Locate and identify every blood parasite.
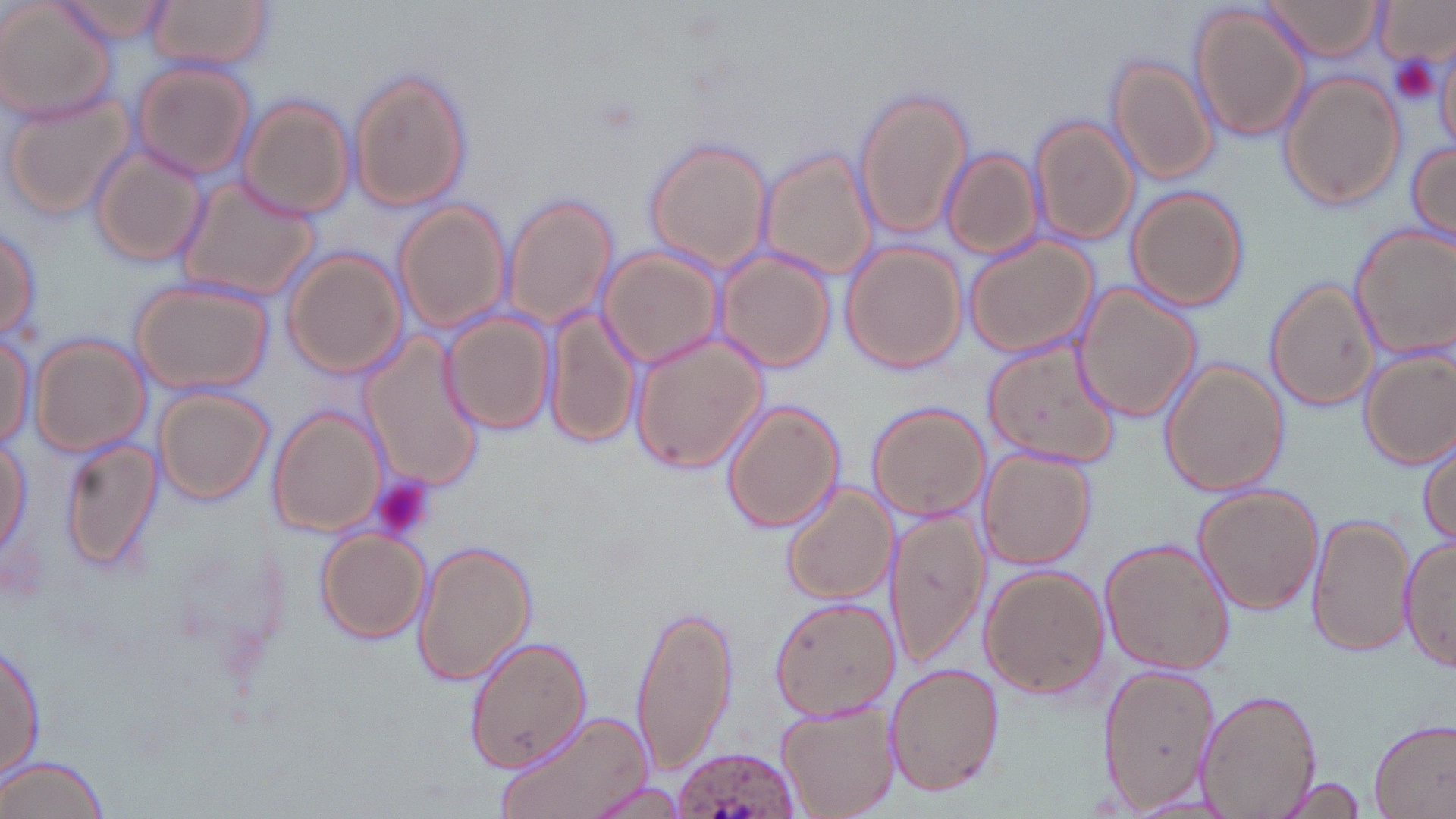
Approximate bounding boxes as (x1, y1, x2, y2) in pixels.
Plasmodium ovale-infected red blood cells: (671, 743, 803, 819).
No Plasmodium falciparum, Plasmodium malariae, Plasmodium vivax, Babesia divergens, or Trypanosoma brucei observed.

Summary:
  - Platelet locations: (1390, 55, 1441, 105), (370, 477, 437, 543)
  - Uninfected red blood cell locations: (149, 0, 271, 71), (1259, 0, 1386, 62), (0, 2, 118, 124), (59, 2, 173, 47), (1374, 2, 1452, 67), (1187, 3, 1312, 143), (1106, 53, 1219, 187), (130, 58, 258, 180), (346, 67, 473, 213), (1278, 71, 1406, 211), (853, 86, 974, 240), (2, 92, 136, 220), (236, 93, 356, 221), (1029, 114, 1139, 248), (642, 138, 774, 275), (89, 143, 209, 269), (1406, 143, 1455, 248), (761, 145, 878, 283), (943, 149, 1042, 262), (175, 174, 321, 302), (1125, 185, 1250, 313), (504, 193, 616, 330), (393, 199, 511, 334), (1349, 223, 1456, 360), (1, 224, 43, 340), (963, 233, 1097, 357), (840, 242, 968, 375), (599, 247, 725, 368), (713, 247, 835, 374), (282, 248, 406, 380), (129, 278, 275, 394), (1265, 278, 1378, 415), (1070, 283, 1203, 423), (545, 304, 641, 450), (442, 309, 555, 435), (628, 326, 769, 475), (0, 329, 35, 448), (359, 330, 486, 493), (28, 332, 152, 458), (982, 336, 1121, 470), (1359, 349, 1456, 469), (1159, 358, 1289, 499), (153, 385, 274, 504), (721, 398, 845, 535), (867, 401, 990, 520), (269, 405, 387, 537), (0, 428, 31, 564), (1416, 431, 1455, 552), (58, 436, 163, 577), (979, 447, 1095, 570), (781, 481, 895, 605), (1194, 484, 1324, 614), (883, 504, 989, 669), (1307, 510, 1412, 661), (314, 528, 431, 643), (1399, 534, 1456, 673), (410, 538, 537, 690), (1100, 538, 1235, 676), (980, 564, 1109, 700), (768, 596, 898, 722), (628, 602, 741, 781), (463, 633, 593, 773), (2, 641, 46, 779), (883, 660, 1003, 797), (1096, 661, 1220, 812), (1196, 688, 1321, 818), (775, 701, 897, 818), (492, 709, 654, 819), (1368, 717, 1456, 819), (2, 753, 112, 819), (1277, 774, 1369, 817), (579, 781, 694, 818)
  - Slide-level diagnosis: Plasmodium ovale
  - Magnification: 1000x
  - Preparation: thin blood smear
  - Modality: optical microscopy
  - Field of view: single
  - Stain: May-Grünwald-Giemsa
  - Image size: 1456×819 pixels